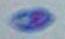 Toxoplasma gondii is shown. Captured at 1000x magnification. Photomicrograph.